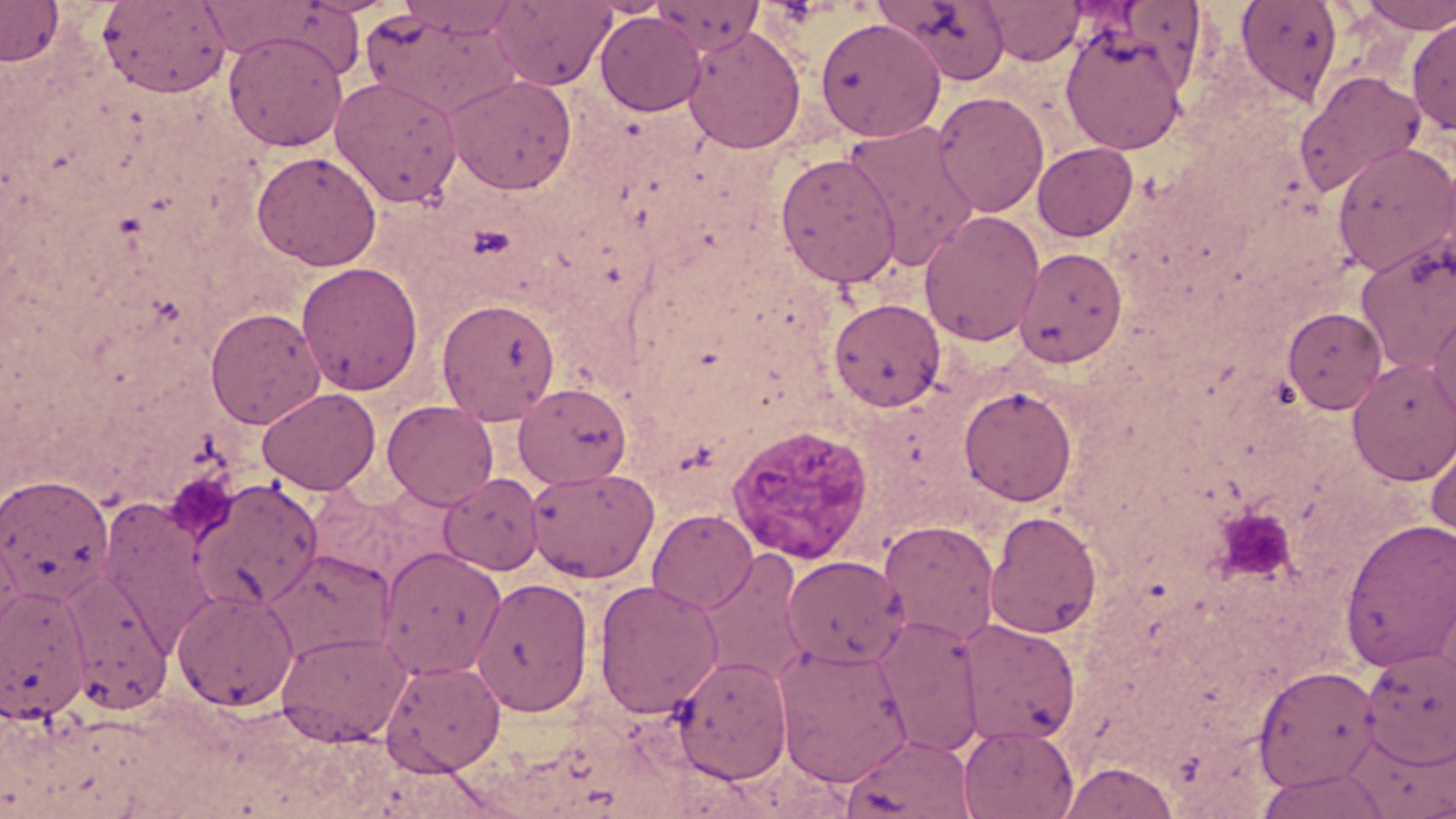
Summary:
  - Coordinate format: approximate bounding boxes as named x1/y1/x2/y2 corners in pixels
  - Uninfected red blood cell locations: (x1=0, y1=0, x2=64, y2=66), (x1=396, y1=0, x2=526, y2=39), (x1=489, y1=0, x2=616, y2=90), (x1=649, y1=0, x2=767, y2=56), (x1=877, y1=0, x2=1012, y2=85), (x1=980, y1=0, x2=1086, y2=66), (x1=1235, y1=0, x2=1343, y2=104), (x1=97, y1=1, x2=232, y2=98), (x1=1357, y1=1, x2=1456, y2=34), (x1=362, y1=8, x2=522, y2=118), (x1=594, y1=12, x2=706, y2=116), (x1=815, y1=17, x2=946, y2=142), (x1=1407, y1=17, x2=1456, y2=135), (x1=682, y1=25, x2=806, y2=154), (x1=1059, y1=26, x2=1190, y2=154), (x1=224, y1=32, x2=347, y2=151), (x1=1295, y1=69, x2=1426, y2=198), (x1=445, y1=73, x2=577, y2=194), (x1=330, y1=75, x2=462, y2=207), (x1=932, y1=91, x2=1050, y2=217), (x1=841, y1=119, x2=982, y2=270), (x1=1332, y1=141, x2=1456, y2=277), (x1=1032, y1=142, x2=1138, y2=241), (x1=252, y1=150, x2=382, y2=270), (x1=775, y1=152, x2=903, y2=288), (x1=1435, y1=157, x2=1456, y2=287), (x1=918, y1=210, x2=1046, y2=347), (x1=1355, y1=232, x2=1456, y2=372), (x1=1014, y1=247, x2=1128, y2=366), (x1=296, y1=261, x2=423, y2=396), (x1=436, y1=297, x2=560, y2=424), (x1=829, y1=298, x2=946, y2=411), (x1=1428, y1=299, x2=1456, y2=427), (x1=205, y1=307, x2=325, y2=429), (x1=1282, y1=307, x2=1387, y2=413), (x1=1348, y1=358, x2=1456, y2=485), (x1=514, y1=382, x2=632, y2=487), (x1=958, y1=385, x2=1077, y2=506), (x1=257, y1=387, x2=381, y2=495), (x1=383, y1=400, x2=499, y2=510), (x1=1426, y1=430, x2=1456, y2=547), (x1=525, y1=467, x2=660, y2=583), (x1=438, y1=472, x2=544, y2=575), (x1=0, y1=474, x2=115, y2=607), (x1=188, y1=478, x2=323, y2=611), (x1=97, y1=500, x2=221, y2=650), (x1=647, y1=508, x2=758, y2=614), (x1=985, y1=510, x2=1103, y2=639), (x1=1340, y1=517, x2=1456, y2=671), (x1=879, y1=519, x2=1000, y2=647), (x1=0, y1=529, x2=24, y2=641), (x1=377, y1=546, x2=506, y2=679), (x1=262, y1=549, x2=396, y2=664), (x1=697, y1=549, x2=812, y2=688), (x1=782, y1=555, x2=909, y2=669), (x1=63, y1=570, x2=173, y2=713), (x1=471, y1=576, x2=594, y2=717), (x1=593, y1=579, x2=724, y2=718), (x1=0, y1=583, x2=93, y2=723), (x1=172, y1=588, x2=299, y2=711), (x1=872, y1=616, x2=986, y2=757), (x1=957, y1=618, x2=1080, y2=746), (x1=276, y1=629, x2=411, y2=745), (x1=772, y1=642, x2=913, y2=787), (x1=1358, y1=645, x2=1456, y2=766), (x1=673, y1=654, x2=792, y2=784), (x1=381, y1=658, x2=505, y2=775), (x1=1253, y1=665, x2=1380, y2=791), (x1=958, y1=724, x2=1079, y2=819), (x1=841, y1=733, x2=976, y2=819), (x1=1057, y1=760, x2=1180, y2=818), (x1=1257, y1=770, x2=1391, y2=819)
  - Platelet locations: (x1=165, y1=473, x2=235, y2=540), (x1=1215, y1=506, x2=1297, y2=584)
  - Plasmodium vivax-infected red blood cell locations: (x1=726, y1=423, x2=874, y2=565)
  - Slide-level diagnosis: Plasmodium vivax
  - Preparation: thin blood smear
  - Image size: 1456×819 pixels
  - Magnification: 1000x
  - Field of view: one of a larger specimen
  - Modality: light microscopy
  - Stain: May-Grünwald-Giemsa